Locate every uninfected red blood cell.
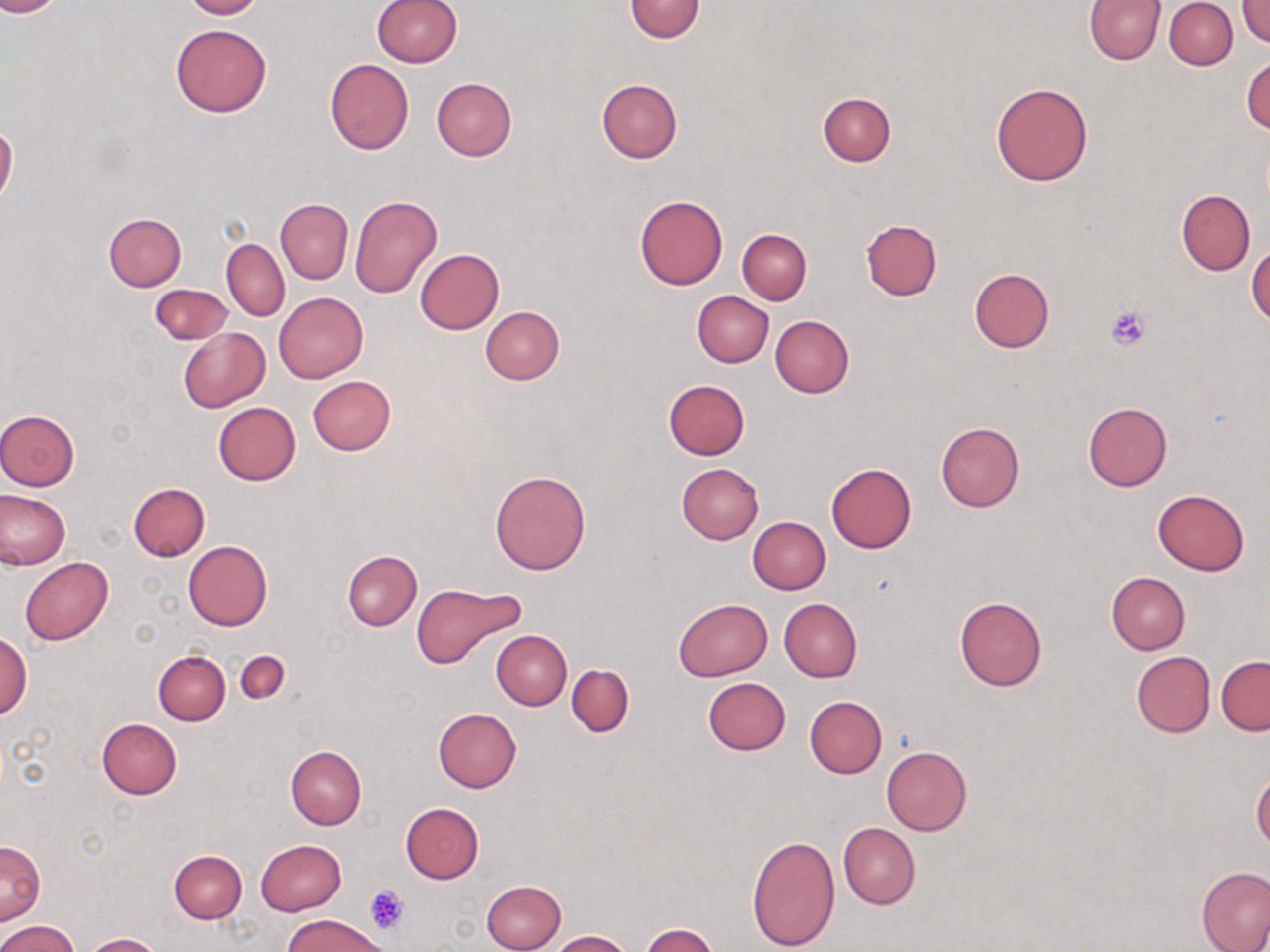
Approximate bounding boxes as [x1, y1, x2, y2] in pixels.
Uninfected red blood cells: [0, 0, 62, 16], [182, 0, 266, 19], [371, 0, 461, 69], [625, 0, 704, 42], [1085, 0, 1165, 64], [1238, 0, 1270, 46], [1164, 1, 1237, 69], [170, 23, 272, 117], [1243, 57, 1270, 133], [324, 58, 414, 154], [431, 78, 516, 161], [596, 79, 682, 163], [990, 81, 1095, 186], [817, 93, 895, 167], [0, 123, 18, 204], [1177, 189, 1255, 275], [634, 195, 728, 290], [349, 196, 443, 299], [276, 199, 352, 284], [104, 212, 187, 291], [860, 219, 941, 301], [737, 228, 812, 304], [221, 240, 289, 321], [1247, 244, 1270, 324], [415, 248, 504, 333], [969, 269, 1054, 353], [149, 283, 233, 344], [693, 291, 774, 367], [274, 292, 367, 383], [479, 306, 564, 385], [770, 315, 854, 398], [178, 328, 270, 412], [308, 376, 395, 456], [662, 378, 750, 460], [1083, 401, 1172, 491], [213, 402, 300, 486], [0, 409, 80, 490], [935, 422, 1025, 512], [676, 463, 763, 544], [826, 463, 917, 553], [489, 470, 591, 574], [129, 482, 210, 561], [1152, 489, 1250, 575], [1, 491, 70, 569], [748, 517, 830, 594], [182, 541, 271, 631], [342, 552, 421, 630], [20, 557, 113, 645], [1106, 571, 1190, 654], [411, 583, 523, 669], [955, 597, 1047, 691], [673, 598, 773, 681], [780, 598, 862, 682], [491, 630, 571, 710], [0, 631, 33, 720], [235, 650, 290, 705], [153, 651, 230, 725], [1131, 652, 1215, 737], [1216, 656, 1270, 735], [567, 664, 633, 737], [702, 677, 791, 755], [805, 696, 887, 778], [433, 709, 522, 792], [95, 719, 181, 799], [286, 745, 367, 829], [881, 746, 971, 835], [1251, 773, 1270, 849], [400, 804, 483, 884], [837, 822, 920, 909], [746, 834, 840, 951], [0, 840, 45, 925], [255, 840, 347, 915], [170, 850, 247, 922], [1196, 867, 1270, 952], [481, 880, 566, 952], [285, 912, 389, 952], [0, 919, 81, 952], [639, 924, 720, 952], [549, 930, 633, 952], [85, 932, 161, 951].

Platelet locations: [1104, 304, 1151, 351], [364, 885, 408, 935]. Slide-level diagnosis: negative for blood parasites. Single field of view. May-Grünwald-Giemsa-stained preparation. Optical microscopy. Image is 1270×952 pixels. Captured at 1000x magnification. Thin blood smear.